Give the extent of all Plasmodium vivax-infected red blood cells.
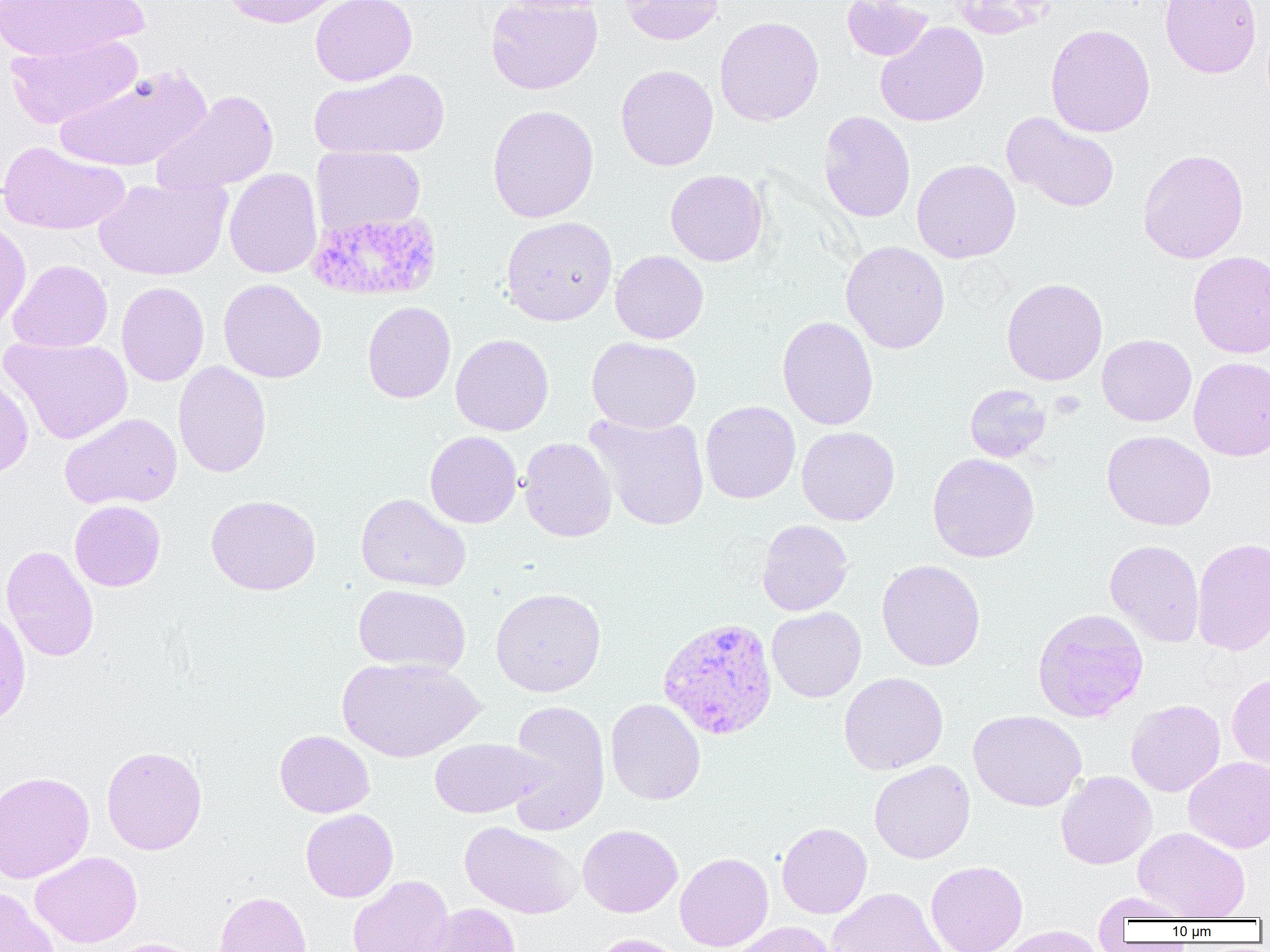

Approximate bounding boxes as (x1, y1, x2, y2) in pixels.
Plasmodium vivax-infected red blood cells: (307, 210, 441, 301), (657, 617, 778, 740).

Summary:
  - Uninfected red blood cell locations: (0, 0, 148, 62), (220, 0, 346, 28), (310, 0, 417, 86), (485, 0, 603, 95), (495, 0, 609, 14), (620, 0, 724, 45), (842, 0, 933, 63), (945, 0, 1056, 39), (1160, 0, 1262, 78), (715, 16, 824, 126), (876, 21, 989, 127), (1045, 24, 1155, 138), (4, 34, 143, 129), (615, 64, 718, 171), (53, 66, 211, 172), (310, 68, 450, 159), (152, 90, 280, 196), (487, 105, 599, 223), (818, 111, 915, 223), (1002, 112, 1120, 213), (0, 141, 130, 236), (311, 145, 425, 236), (1137, 148, 1249, 263), (911, 159, 1021, 263), (224, 168, 322, 279), (665, 169, 768, 266), (94, 175, 231, 281), (500, 216, 617, 326), (0, 218, 31, 332), (841, 240, 950, 353), (610, 250, 709, 344), (1188, 250, 1270, 359), (8, 259, 112, 353), (1001, 278, 1108, 386), (218, 279, 327, 383), (116, 282, 209, 386), (362, 301, 455, 404), (777, 316, 879, 430), (451, 334, 553, 436), (1097, 334, 1196, 426), (1, 336, 133, 444), (586, 336, 701, 433), (1189, 356, 1270, 461), (173, 361, 272, 478), (0, 369, 34, 478), (965, 384, 1051, 462), (700, 400, 801, 504), (60, 413, 183, 510), (586, 413, 710, 531), (797, 426, 899, 526), (1102, 430, 1216, 531), (425, 431, 522, 528), (518, 437, 617, 542), (927, 452, 1040, 563), (355, 493, 471, 592), (206, 494, 321, 596), (69, 500, 166, 591), (756, 519, 853, 616), (1192, 537, 1270, 656), (1104, 539, 1205, 647), (1, 544, 99, 662), (877, 559, 985, 671), (353, 584, 470, 675), (490, 587, 606, 697), (0, 603, 31, 728), (767, 607, 866, 702), (1032, 608, 1149, 723), (336, 656, 483, 762), (838, 672, 948, 774), (1227, 673, 1270, 771), (606, 698, 706, 805), (504, 699, 611, 836), (1125, 699, 1225, 797), (968, 710, 1087, 812), (275, 729, 375, 817), (429, 738, 544, 818), (101, 745, 207, 855), (1184, 757, 1270, 853), (869, 760, 975, 863), (0, 771, 94, 883), (1055, 771, 1157, 870), (301, 809, 398, 902), (460, 821, 582, 918), (776, 822, 872, 918), (577, 824, 682, 917), (1134, 827, 1250, 921), (30, 851, 143, 948), (675, 852, 773, 951), (926, 860, 1028, 952), (348, 875, 454, 952), (827, 886, 947, 952), (0, 887, 59, 952), (213, 890, 312, 952), (1092, 892, 1195, 923), (422, 903, 522, 952), (728, 921, 837, 952), (991, 925, 1110, 952), (588, 933, 688, 952), (101, 938, 203, 952)
  - Slide-level diagnosis: Plasmodium vivax
  - Preparation: thin blood smear
  - Modality: optical microscopy
  - Magnification: 1000x
  - Image size: 1270×952 pixels
  - Field of view: single